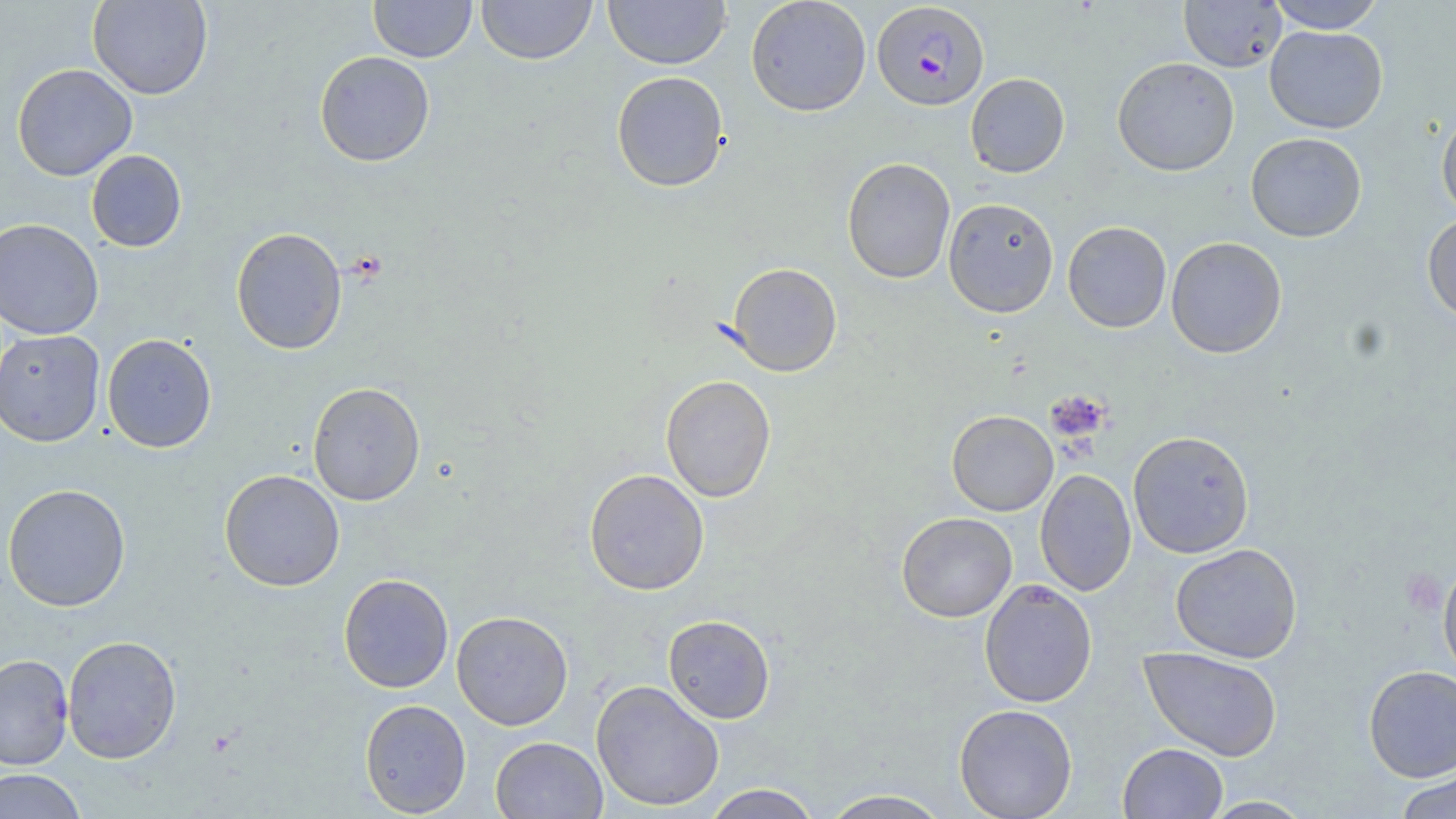
{
  "slide_level_diagnosis": "Plasmodium falciparum",
  "field_of_view": "one of a larger specimen",
  "plasmodium_falciparum_infected_red_blood_cell_locations": "approximate bounding boxes as (x1, y1, x2, y2) in pixels: (871, 2, 989, 111)",
  "platelet_locations": "approximate bounding boxes as (x1, y1, x2, y2) in pixels: (1046, 389, 1112, 445)",
  "preparation": "thin blood film",
  "image_size": "1456×819 pixels",
  "stain": "May-Grünwald-Giemsa",
  "uninfected_red_blood_cell_locations": "approximate bounding boxes as (x1, y1, x2, y2) in pixels: (88, 0, 213, 100), (368, 0, 476, 62), (476, 0, 597, 65), (603, 0, 731, 70), (745, 0, 871, 116), (1266, 0, 1387, 33), (1179, 1, 1286, 72), (1264, 26, 1387, 133), (314, 50, 435, 168), (1112, 57, 1240, 176), (12, 63, 137, 181), (611, 71, 730, 192), (965, 73, 1069, 178), (1436, 108, 1456, 220), (1245, 132, 1367, 242), (86, 150, 187, 252), (842, 157, 956, 284), (943, 197, 1059, 318), (1422, 213, 1456, 324), (0, 218, 104, 340), (1062, 221, 1172, 333), (231, 227, 347, 355), (1166, 236, 1287, 358), (726, 262, 842, 377), (0, 329, 105, 447), (102, 333, 217, 453), (660, 375, 776, 502), (308, 382, 425, 506), (946, 410, 1058, 516), (1128, 430, 1254, 558), (584, 468, 710, 596), (219, 469, 345, 592), (1035, 469, 1137, 596), (2, 483, 131, 612), (896, 512, 1017, 622), (1169, 543, 1303, 663), (1438, 559, 1456, 684), (338, 573, 454, 694), (978, 579, 1097, 708), (451, 610, 574, 730), (663, 614, 775, 724), (62, 634, 182, 764), (1139, 647, 1283, 761), (0, 653, 74, 770), (1363, 665, 1456, 782), (590, 679, 724, 812), (359, 699, 472, 817), (953, 703, 1078, 819), (490, 736, 608, 819), (1118, 742, 1228, 818), (0, 769, 87, 819), (1393, 769, 1456, 819), (703, 783, 822, 818), (819, 788, 954, 818), (1200, 796, 1315, 818)",
  "modality": "optical microscopy",
  "magnification": "1000x"
}